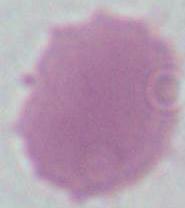

magnification = 1000x
modality = photomicrograph
identification = erythrocyte